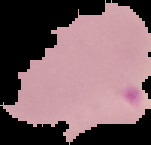 From a thin blood film. Result: Plasmodium parasites identified. Segmented cell region on a black background. Image is 151×145 pixels.